Report the malaria status of this cell.
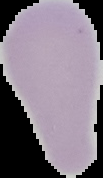

Uninfected.

Summary:
  - Preparation: thin blood smear
  - Image type: cell region segmented out of the field of view; surrounding area masked to black
  - Image size: 103×178 pixels